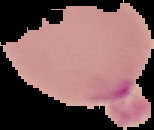
image size = 154×130 pixels
image type = segmented cell region with the area outside set to black
preparation = thin blood film
malaria status = parasitized